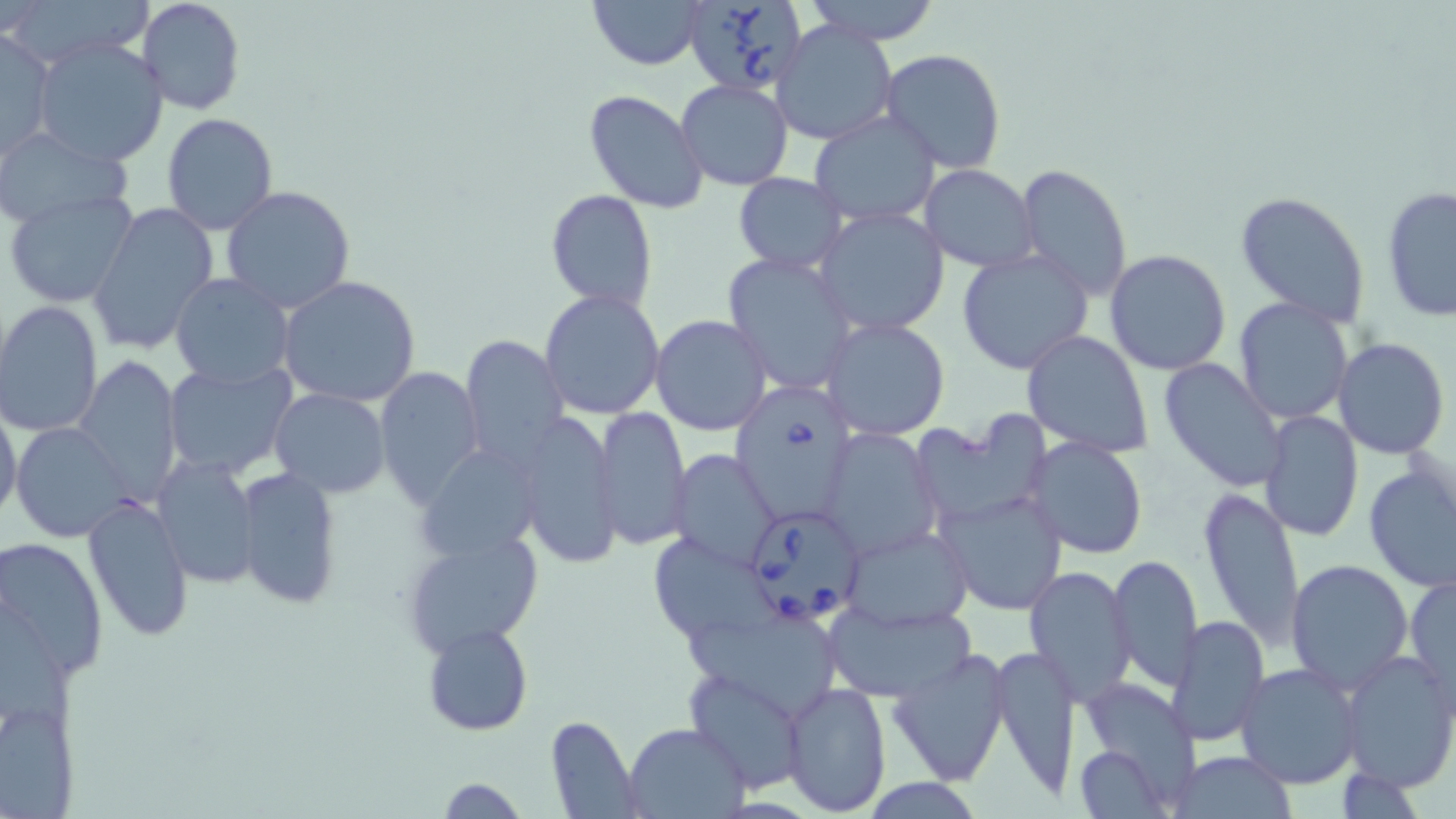
Approximate bounding boxes as named x1/y1/x2/y2 corners in pixels. Uninfected red blood cell locations: (x1=6, y1=0, x2=155, y2=66), (x1=138, y1=0, x2=246, y2=116), (x1=589, y1=0, x2=707, y2=69), (x1=803, y1=0, x2=943, y2=43), (x1=771, y1=19, x2=898, y2=146), (x1=0, y1=28, x2=55, y2=161), (x1=32, y1=38, x2=169, y2=168), (x1=880, y1=49, x2=1006, y2=175), (x1=719, y1=61, x2=864, y2=188), (x1=676, y1=79, x2=793, y2=190), (x1=584, y1=89, x2=710, y2=212), (x1=810, y1=111, x2=941, y2=229), (x1=160, y1=112, x2=279, y2=235), (x1=0, y1=126, x2=131, y2=229), (x1=181, y1=129, x2=316, y2=289), (x1=919, y1=164, x2=1038, y2=272), (x1=1016, y1=164, x2=1133, y2=298), (x1=733, y1=174, x2=847, y2=274), (x1=1380, y1=185, x2=1455, y2=324), (x1=222, y1=186, x2=356, y2=316), (x1=3, y1=188, x2=139, y2=309), (x1=545, y1=189, x2=659, y2=313), (x1=1234, y1=191, x2=1371, y2=327), (x1=86, y1=201, x2=221, y2=353), (x1=815, y1=207, x2=950, y2=337), (x1=956, y1=249, x2=1093, y2=375), (x1=1104, y1=249, x2=1232, y2=377), (x1=722, y1=252, x2=858, y2=395), (x1=169, y1=273, x2=294, y2=387), (x1=278, y1=274, x2=422, y2=409), (x1=540, y1=289, x2=666, y2=420), (x1=1232, y1=297, x2=1356, y2=426), (x1=1, y1=302, x2=103, y2=437), (x1=651, y1=314, x2=773, y2=435), (x1=821, y1=317, x2=951, y2=440), (x1=1020, y1=330, x2=1153, y2=457), (x1=461, y1=334, x2=569, y2=466), (x1=1333, y1=338, x2=1449, y2=459), (x1=74, y1=355, x2=182, y2=499), (x1=1157, y1=358, x2=1290, y2=492), (x1=163, y1=360, x2=299, y2=480), (x1=374, y1=365, x2=485, y2=507), (x1=269, y1=388, x2=389, y2=497), (x1=0, y1=398, x2=22, y2=529), (x1=595, y1=405, x2=691, y2=550), (x1=1259, y1=410, x2=1364, y2=543), (x1=512, y1=412, x2=620, y2=570), (x1=919, y1=415, x2=1054, y2=520), (x1=12, y1=420, x2=129, y2=543), (x1=1290, y1=420, x2=1410, y2=559), (x1=819, y1=426, x2=942, y2=559), (x1=1026, y1=437, x2=1149, y2=560), (x1=418, y1=451, x2=542, y2=562), (x1=669, y1=451, x2=781, y2=569), (x1=152, y1=454, x2=259, y2=587), (x1=1362, y1=463, x2=1456, y2=593), (x1=233, y1=465, x2=343, y2=612), (x1=1197, y1=487, x2=1304, y2=646), (x1=937, y1=489, x2=1067, y2=616), (x1=82, y1=494, x2=194, y2=642), (x1=840, y1=524, x2=972, y2=631), (x1=402, y1=529, x2=545, y2=658), (x1=649, y1=532, x2=771, y2=644), (x1=0, y1=534, x2=109, y2=679), (x1=1109, y1=553, x2=1203, y2=687), (x1=1287, y1=559, x2=1413, y2=692), (x1=1024, y1=565, x2=1136, y2=704), (x1=1406, y1=573, x2=1456, y2=706), (x1=823, y1=597, x2=976, y2=702), (x1=1167, y1=615, x2=1269, y2=748), (x1=679, y1=617, x2=844, y2=724), (x1=424, y1=622, x2=531, y2=735), (x1=989, y1=640, x2=1080, y2=802), (x1=886, y1=646, x2=1013, y2=788), (x1=1338, y1=650, x2=1456, y2=794), (x1=1235, y1=663, x2=1364, y2=789), (x1=685, y1=668, x2=806, y2=793), (x1=781, y1=679, x2=890, y2=815), (x1=1070, y1=685, x2=1200, y2=819), (x1=2, y1=696, x2=79, y2=819), (x1=544, y1=715, x2=642, y2=819), (x1=625, y1=722, x2=749, y2=818), (x1=1073, y1=745, x2=1173, y2=816), (x1=1169, y1=751, x2=1298, y2=818), (x1=435, y1=777, x2=528, y2=818), (x1=858, y1=778, x2=989, y2=816). Babesia divergens-infected red blood cell locations: (x1=685, y1=0, x2=808, y2=97), (x1=728, y1=383, x2=853, y2=520), (x1=743, y1=505, x2=866, y2=626). Slide-level diagnosis: Babesia divergens. Thin blood smear. 1000x magnification. Light microscopy. One field of a larger specimen. Image is 1456×819 pixels. May-Grünwald-Giemsa stain.